Assess this cell for malaria.
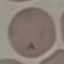

It is uninfected.

preparation = thin blood smear
image type = cell patch, automatically extracted from a larger field of view and resized to 64 × 64 pixels
capture = smartphone camera at the microscope eyepiece
stain = Giemsa